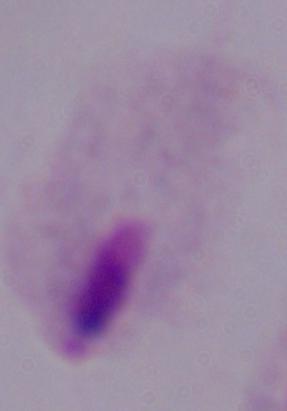

Summary:
  - Identification: trichomonad
  - Magnification: 1000x
  - Modality: micrograph